Comment on the morphology of the erythrocytes.
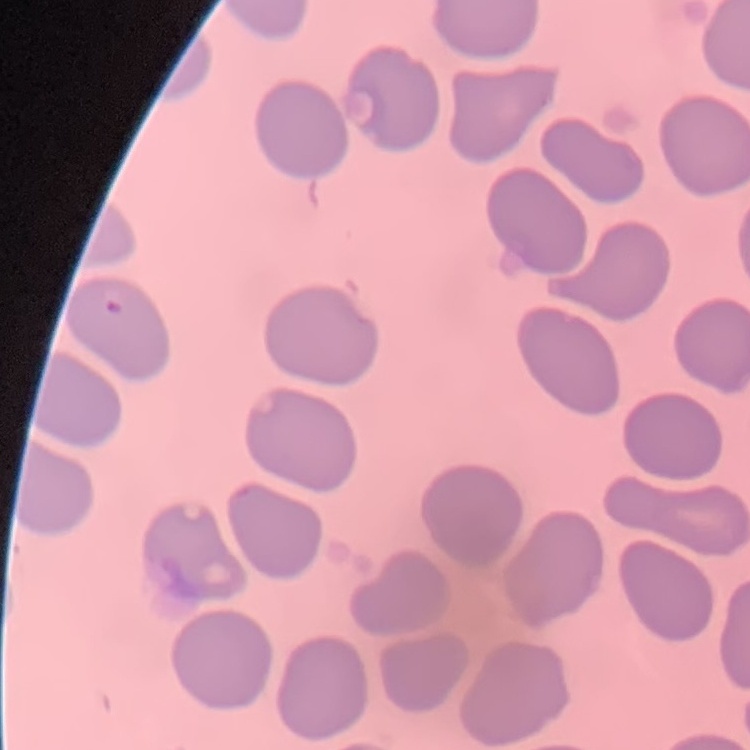
They show no rouleaux formation.

preparation = thin blood film
image type = square crop of a larger photomicrograph
stain = Field's or Giemsa